Report the malaria status of this cell.
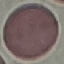

Uninfected.

Photographed with a smartphone camera at the microscope eyepiece. Giemsa-stained preparation. Automatically extracted cell patch, resized to 64 × 64 pixels. Thin blood film.